Assess the morphology of the red blood cells.
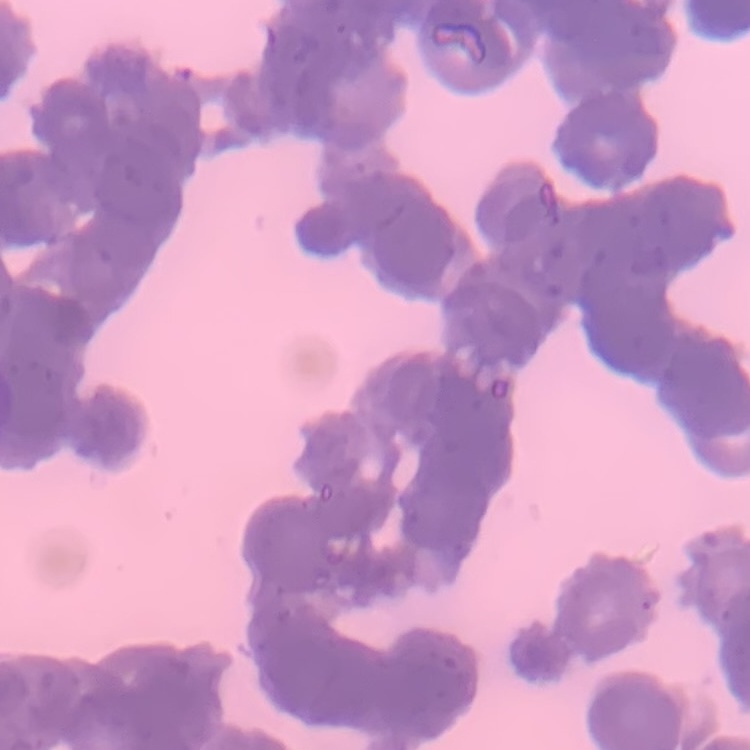

Rouleaux formation.

preparation = thin blood film
image type = square crop of a larger photomicrograph
stain = Field's or Giemsa